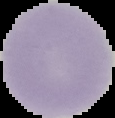
Summary:
  - Image type: cell region segmented out of the field of view; surrounding area masked to black
  - Preparation: thin blood film
  - Image size: 115×118 pixels
  - Malaria status: uninfected